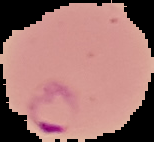

Malaria status: parasitized. Image is 154×142 pixels. The area outside the segmented cell region is set to black. From a thin blood smear.